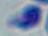

Toxoplasma gondii is seen. 1000x magnification. Micrograph.